Describe the morphology of the red blood cells.
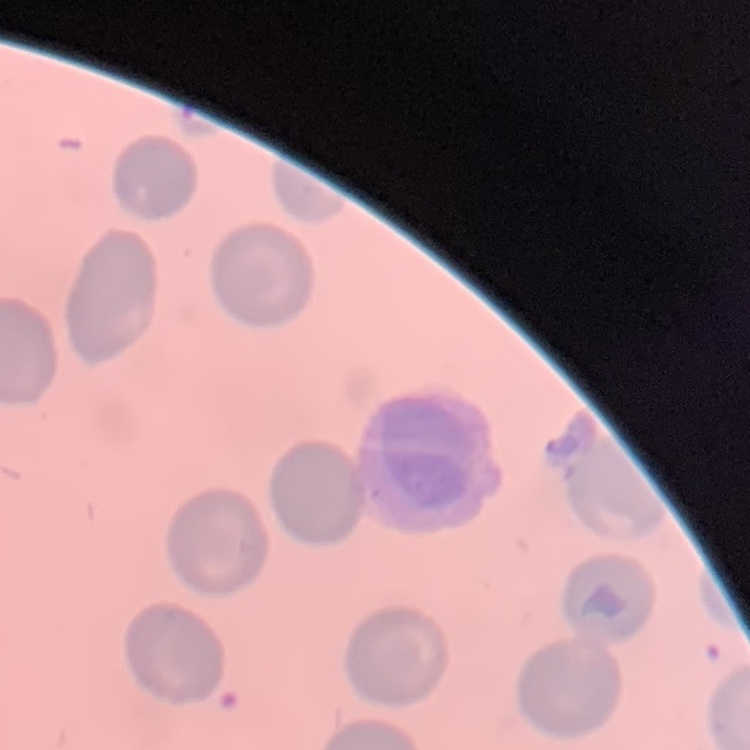
They show no rouleaux formation.

Thin blood smear. One tile cut from a larger photomicrograph. Stained with either Field's or Giemsa.